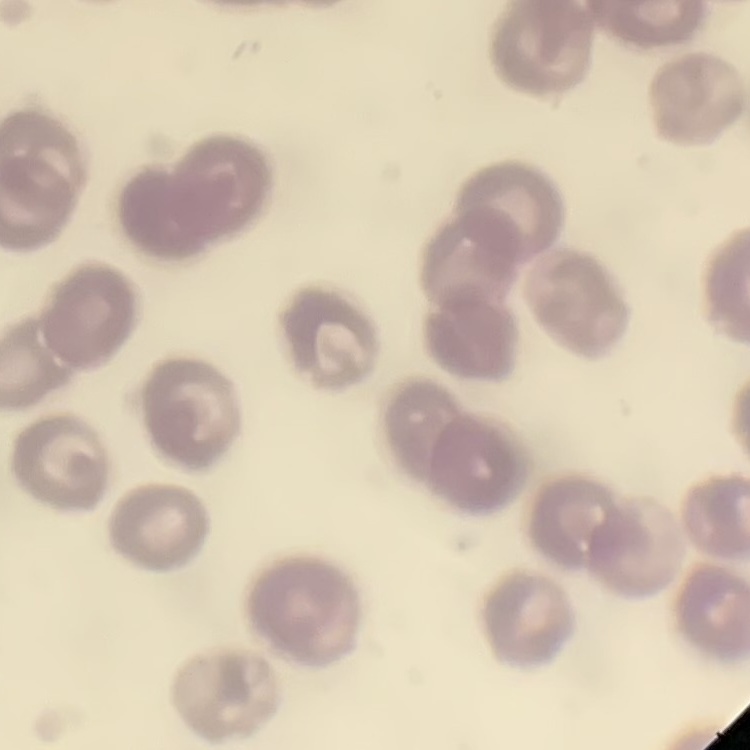
{
  "red_blood_cell_morphology": "no rouleaux formation",
  "preparation": "thin blood smear",
  "image_type": "one tile cut from a larger photomicrograph",
  "stain": "Field's or Giemsa"
}